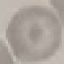

result: no malaria parasites detected
preparation: thin blood smear
image_type: cell patch, automatically extracted from a larger field of view and resized to 64 × 64 pixels
capture: smartphone camera at the microscope eyepiece
stain: Giemsa